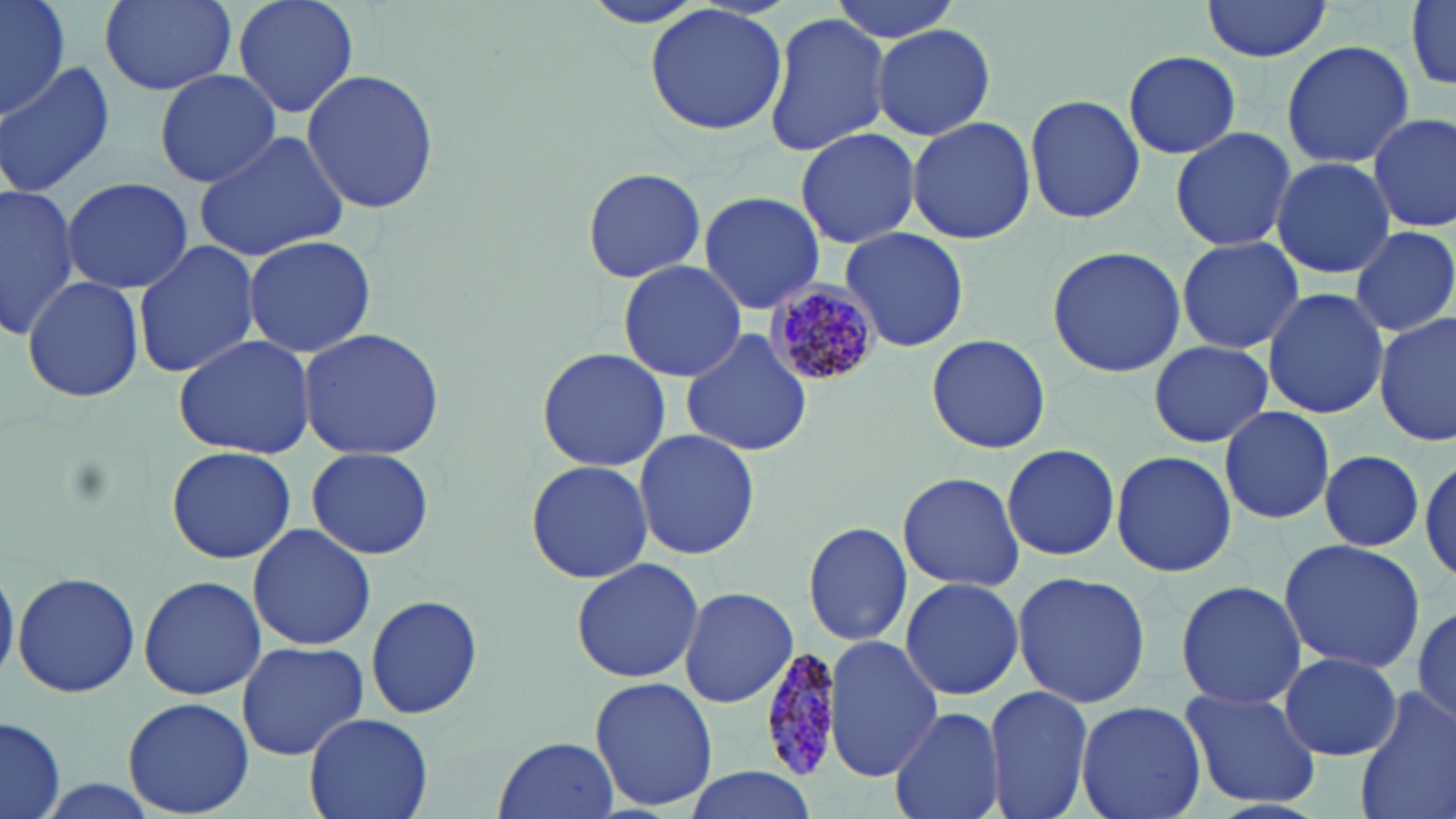
slide-level diagnosis = Plasmodium malariae
stain = May-Grünwald-Giemsa
uninfected red blood cell locations = approximate bounding boxes as named x1/y1/x2/y2 corners in pixels: (x1=0, y1=0, x2=69, y2=121), (x1=101, y1=0, x2=235, y2=95), (x1=231, y1=0, x2=361, y2=121), (x1=825, y1=0, x2=964, y2=44), (x1=1201, y1=0, x2=1334, y2=62), (x1=1408, y1=2, x2=1456, y2=91), (x1=643, y1=4, x2=789, y2=137), (x1=763, y1=11, x2=889, y2=158), (x1=873, y1=24, x2=996, y2=140), (x1=1280, y1=40, x2=1415, y2=170), (x1=1123, y1=51, x2=1241, y2=159), (x1=0, y1=61, x2=116, y2=195), (x1=153, y1=68, x2=281, y2=188), (x1=300, y1=69, x2=441, y2=216), (x1=1024, y1=92, x2=1144, y2=224), (x1=1369, y1=111, x2=1455, y2=234), (x1=907, y1=116, x2=1036, y2=245), (x1=1168, y1=125, x2=1296, y2=251), (x1=795, y1=127, x2=920, y2=247), (x1=192, y1=128, x2=352, y2=261), (x1=1270, y1=155, x2=1394, y2=280), (x1=582, y1=166, x2=706, y2=283), (x1=62, y1=176, x2=193, y2=295), (x1=0, y1=182, x2=80, y2=339), (x1=698, y1=191, x2=825, y2=314), (x1=1350, y1=224, x2=1456, y2=338), (x1=840, y1=227, x2=970, y2=353), (x1=242, y1=234, x2=376, y2=356), (x1=1176, y1=236, x2=1304, y2=354), (x1=132, y1=240, x2=262, y2=379), (x1=1046, y1=243, x2=1186, y2=379), (x1=618, y1=260, x2=744, y2=382), (x1=21, y1=274, x2=144, y2=403), (x1=1261, y1=286, x2=1389, y2=421), (x1=1375, y1=314, x2=1453, y2=448), (x1=681, y1=327, x2=812, y2=458), (x1=295, y1=328, x2=446, y2=460), (x1=172, y1=333, x2=319, y2=460), (x1=925, y1=333, x2=1052, y2=455), (x1=1147, y1=340, x2=1273, y2=449), (x1=537, y1=347, x2=670, y2=471), (x1=1218, y1=405, x2=1337, y2=526), (x1=633, y1=429, x2=761, y2=559), (x1=1001, y1=443, x2=1121, y2=563), (x1=165, y1=445, x2=296, y2=565), (x1=305, y1=447, x2=435, y2=561), (x1=1318, y1=449, x2=1425, y2=550), (x1=1110, y1=450, x2=1238, y2=577), (x1=1418, y1=452, x2=1455, y2=591), (x1=524, y1=459, x2=655, y2=585), (x1=898, y1=470, x2=1025, y2=592), (x1=804, y1=521, x2=916, y2=649), (x1=247, y1=522, x2=376, y2=650), (x1=1278, y1=537, x2=1427, y2=674), (x1=570, y1=557, x2=704, y2=684), (x1=0, y1=560, x2=18, y2=689), (x1=1011, y1=570, x2=1151, y2=709), (x1=13, y1=571, x2=141, y2=697), (x1=138, y1=575, x2=267, y2=701), (x1=899, y1=576, x2=1026, y2=701), (x1=1174, y1=579, x2=1309, y2=711), (x1=677, y1=586, x2=798, y2=708), (x1=366, y1=594, x2=484, y2=721), (x1=1411, y1=603, x2=1456, y2=730), (x1=824, y1=639, x2=944, y2=779), (x1=234, y1=641, x2=368, y2=760), (x1=1279, y1=652, x2=1402, y2=761), (x1=589, y1=676, x2=716, y2=812), (x1=984, y1=684, x2=1094, y2=819), (x1=1178, y1=686, x2=1323, y2=810), (x1=1354, y1=687, x2=1456, y2=819), (x1=121, y1=696, x2=255, y2=818), (x1=1074, y1=700, x2=1208, y2=819), (x1=887, y1=707, x2=1004, y2=819), (x1=303, y1=712, x2=433, y2=819), (x1=0, y1=717, x2=64, y2=818), (x1=493, y1=733, x2=617, y2=816), (x1=680, y1=767, x2=818, y2=819)
magnification = 1000x
preparation = thin blood smear
Plasmodium malariae-infected red blood cell locations = approximate bounding boxes as named x1/y1/x2/y2 corners in pixels: (x1=766, y1=283, x2=879, y2=389), (x1=758, y1=647, x2=839, y2=781)
image size = 1456×819 pixels
field of view = single
modality = light microscopy